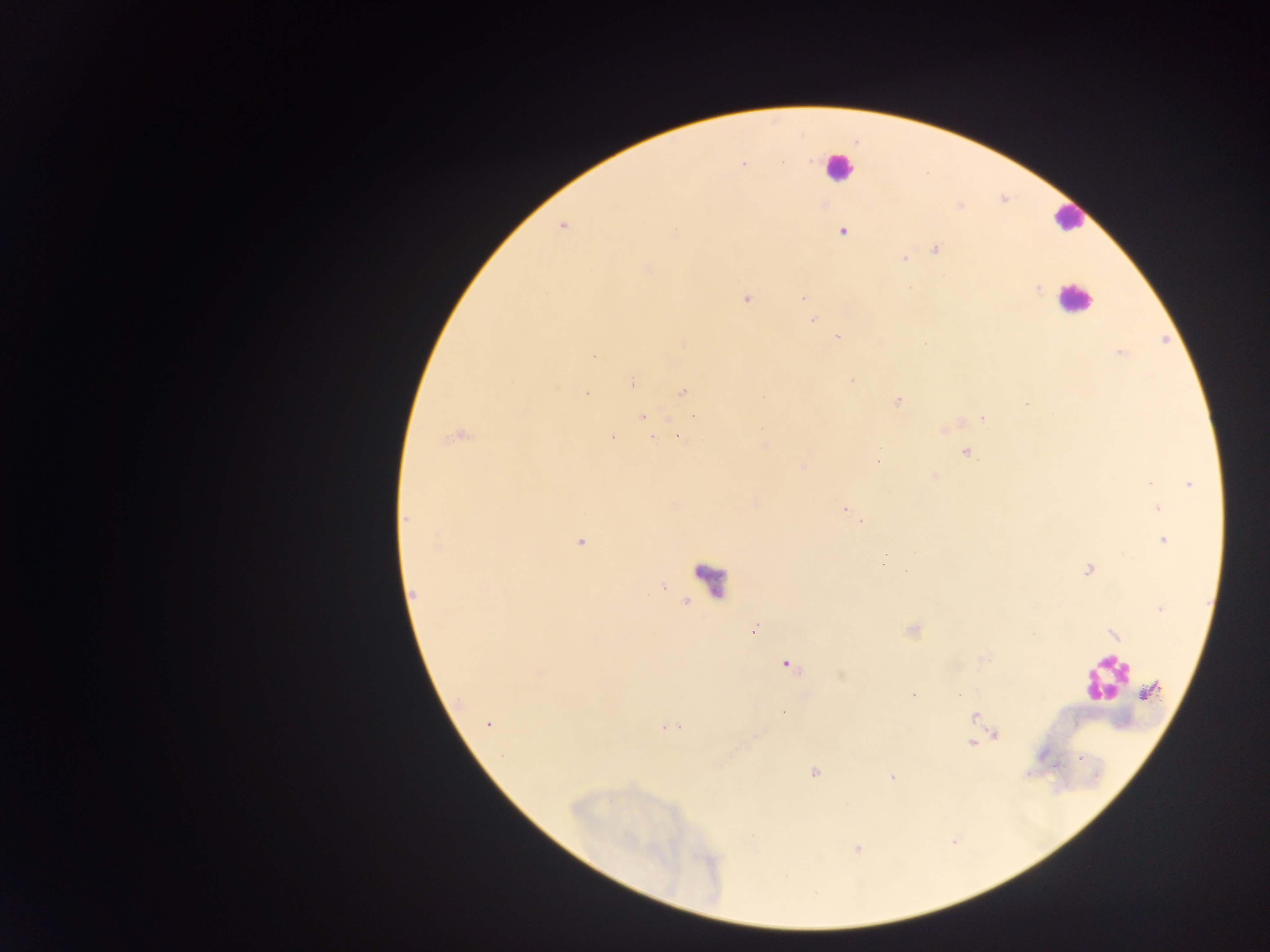

leukocyte_locations: 'approximate centers as {x, y} in pixels: {837, 167}, {1068, 218}, {1075, 299}, {708, 581}, {1105, 678}'
plasmodium_parasite_locations: 'approximate centers as {x, y} in pixels: {743, 164}, {563, 225}, {842, 232}, {676, 234}, {935, 249}, {903, 258}, {646, 268}, {1037, 288}, {802, 297}, {746, 299}, {812, 319}, {837, 336}, {684, 343}, {1121, 352}, {593, 356}, {851, 381}, {632, 382}, {683, 391}, {587, 394}, {898, 400}, {695, 415}, {642, 417}, {982, 418}, {457, 437}, {612, 437}, {680, 438}, {653, 439}, {764, 445}, {966, 453}, {877, 461}, {802, 467}, {933, 475}, {1189, 484}, {1158, 508}, {844, 509}, {406, 519}, {863, 520}, {1164, 541}, {581, 542}, {436, 545}, {883, 562}, {1088, 570}, {413, 594}, {1161, 608}, {753, 630}, {788, 665}, {914, 695}, {959, 695}, {784, 713}, {975, 717}, {488, 724}, {669, 728}, {996, 735}, {971, 743}, {814, 772}, {892, 777}'
image_size: 1270×952 pixels
capture: mobile-phone photograph through a microscope
field_of_view: single
country: Ghana
preparation: thick blood film